Report the malaria status of this cell.
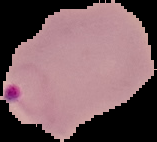

Parasitized.

image size = 157×142 pixels
preparation = thin blood smear
image type = segmented cell region with the area outside set to black